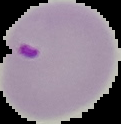
Summary:
  - Image size: 121×124 pixels
  - Image type: cell region segmented out of the field of view; surrounding area masked to black
  - Result: Plasmodium parasites detected
  - Preparation: thin blood smear